Comment on the morphology of the red blood cells.
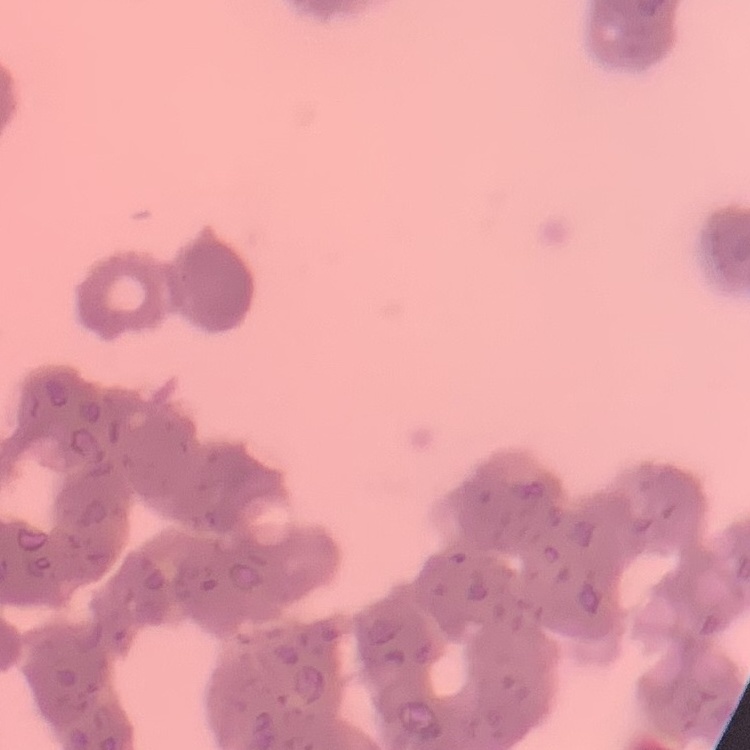
They show rouleaux formation.

preparation = thin blood smear
image type = one tile cut from a larger photomicrograph
stain = Field's or Giemsa